Assess this cell for malaria.
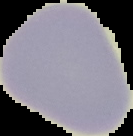
It is uninfected.

Summary:
  - Image size: 133×136 pixels
  - Image type: segmented cell region on a black background
  - Preparation: thin blood film